Assess this cell for malaria.
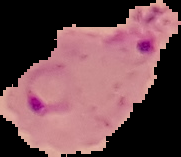

Parasitized.

preparation = thin blood film
image size = 181×157 pixels
image type = cell region segmented out of the field of view; surrounding area masked to black